Outline each blood parasite and name the species.
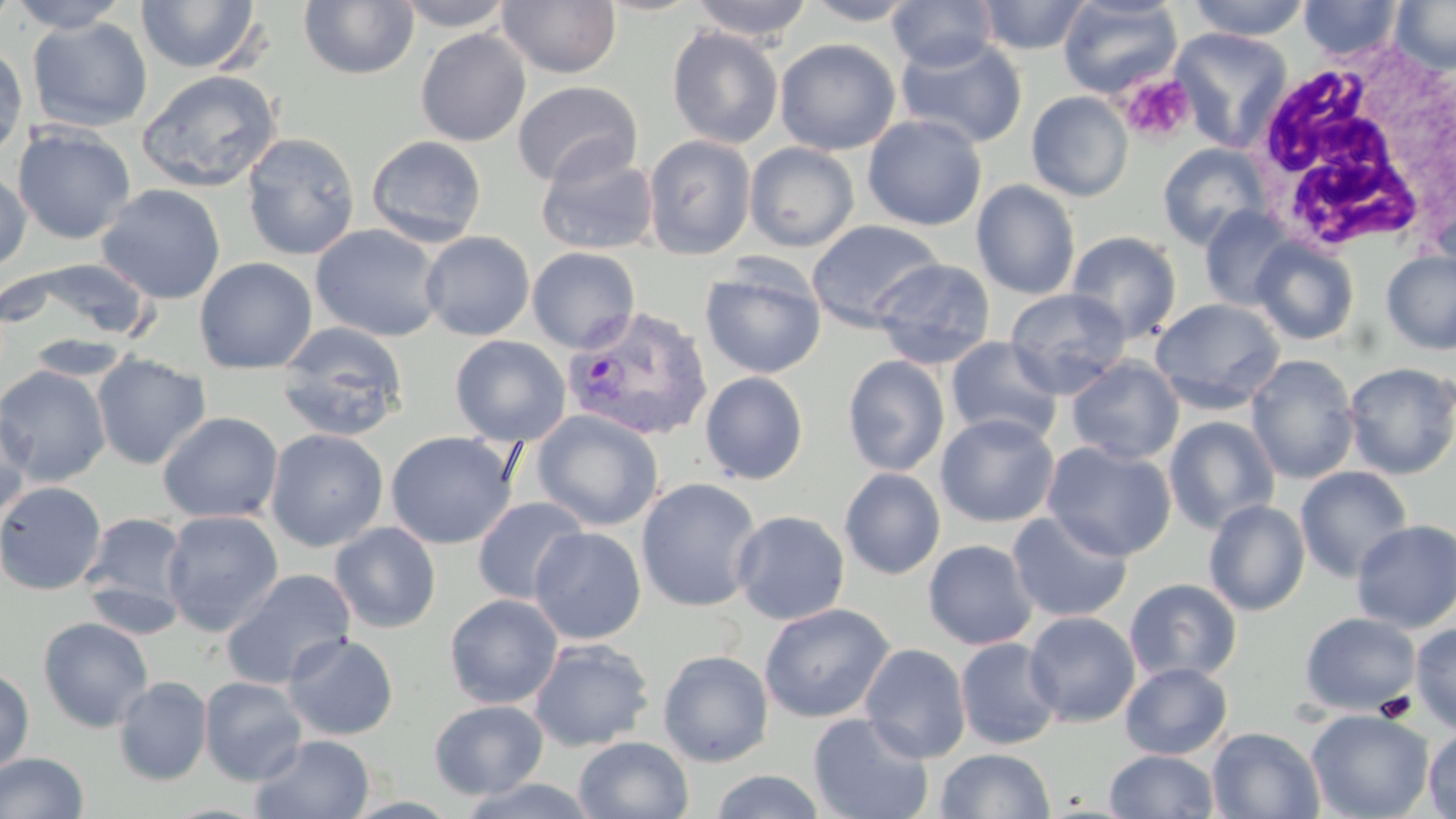

Approximate bounding boxes as [x1, y1, x2, y2] in pixels.
Plasmodium vivax-infected red blood cells: [563, 306, 712, 440].
No Plasmodium falciparum, Plasmodium ovale, Plasmodium malariae, Babesia divergens, or Trypanosoma brucei observed.

Platelet locations: [1120, 73, 1197, 144]. Uninfected red blood cell locations: [0, 0, 19, 32], [6, 0, 133, 32], [136, 0, 262, 74], [392, 0, 516, 31], [497, 0, 622, 79], [690, 0, 814, 41], [887, 0, 999, 71], [976, 0, 1092, 54], [1057, 0, 1182, 98], [1186, 0, 1312, 41], [1298, 0, 1403, 60], [1391, 0, 1456, 74], [299, 1, 419, 80], [800, 1, 922, 25], [27, 17, 152, 133], [666, 25, 784, 149], [1170, 27, 1293, 152], [415, 29, 531, 146], [894, 35, 1028, 149], [774, 38, 900, 156], [0, 43, 28, 162], [136, 70, 282, 193], [512, 80, 642, 189], [1026, 91, 1134, 202], [863, 115, 988, 231], [12, 124, 136, 245], [241, 132, 361, 261], [365, 135, 487, 248], [643, 135, 756, 259], [744, 142, 860, 252], [1157, 142, 1272, 250], [535, 148, 659, 256], [0, 168, 32, 274], [971, 180, 1081, 300], [97, 184, 226, 304], [1200, 206, 1299, 311], [806, 219, 945, 333], [312, 224, 445, 342], [420, 231, 535, 341], [1066, 231, 1182, 343], [1250, 237, 1360, 345], [527, 246, 640, 353], [1381, 250, 1456, 354], [194, 257, 318, 374], [10, 258, 157, 346], [871, 258, 996, 370], [700, 262, 826, 379], [1005, 287, 1132, 399], [1150, 298, 1285, 415], [275, 323, 409, 442], [450, 335, 571, 446], [945, 336, 1064, 445], [91, 353, 211, 470], [1246, 354, 1360, 484], [842, 355, 950, 477], [1066, 357, 1184, 464], [475, 359, 626, 484], [1342, 362, 1456, 480], [0, 365, 111, 487], [700, 371, 809, 485], [0, 398, 34, 521], [532, 409, 664, 531], [157, 412, 283, 523], [936, 413, 1059, 527], [1163, 415, 1281, 535], [266, 428, 388, 553], [385, 431, 518, 550], [1042, 441, 1176, 561], [1295, 465, 1413, 582], [840, 468, 945, 579], [636, 478, 763, 612], [0, 480, 107, 596], [472, 496, 589, 605], [1204, 499, 1311, 616], [160, 510, 284, 635], [732, 510, 850, 625], [80, 511, 191, 628], [1007, 511, 1133, 623], [1350, 519, 1456, 633], [330, 522, 441, 634], [530, 527, 646, 645], [923, 540, 1038, 650], [221, 568, 357, 689], [1124, 578, 1242, 684], [444, 594, 563, 709], [759, 603, 894, 724], [1023, 611, 1141, 727], [1299, 612, 1422, 716], [38, 616, 154, 733], [1409, 622, 1456, 733], [283, 633, 399, 741], [528, 638, 655, 752], [955, 638, 1063, 750], [860, 644, 972, 762], [658, 649, 774, 766], [1120, 662, 1233, 759], [0, 664, 35, 776], [113, 675, 213, 786], [199, 676, 307, 785], [429, 699, 548, 800], [1306, 708, 1434, 819], [808, 712, 935, 819], [1423, 726, 1456, 818], [1207, 727, 1325, 818], [251, 733, 375, 819], [574, 735, 694, 819], [936, 748, 1055, 819], [1104, 749, 1220, 818], [0, 751, 89, 819], [709, 770, 827, 818], [456, 776, 601, 818]. White blood cell locations: [1239, 42, 1456, 258]. Slide-level diagnosis: Plasmodium vivax. 1000x magnification. Image is 1456×819 pixels. May-Grünwald-Giemsa-stained preparation. Optical microscopy. Single field of view. Thin blood film.